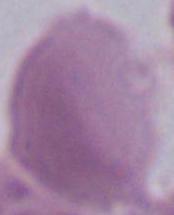 Captured at 1000x magnification. An erythrocyte is shown. Micrograph.